Locate and identify every blood parasite.
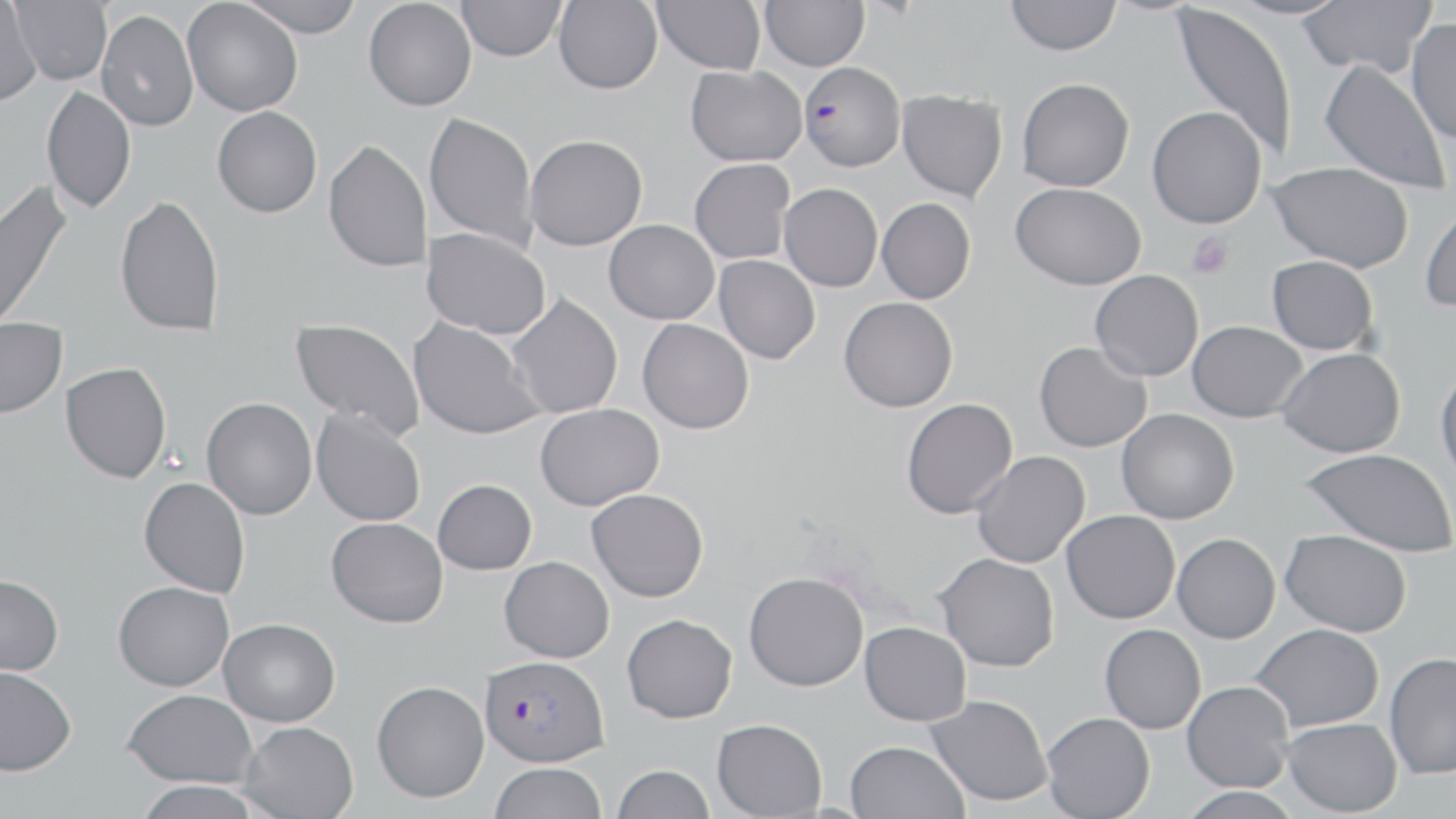
Approximate bounding boxes as (x1,y1)-(x2,y2) corner pairs in pixels.
Plasmodium falciparum-infected red blood cells: (798,61)-(905,171), (479,654)-(609,767).
No Plasmodium ovale, Plasmodium malariae, Plasmodium vivax, Babesia divergens, or Trypanosoma brucei observed.

Uninfected red blood cell locations: (182,0)-(303,116), (238,0)-(364,38), (363,0)-(476,111), (651,0)-(765,75), (760,0)-(869,71), (1005,0)-(1121,56), (1229,0)-(1349,20), (1297,0)-(1436,78), (9,1)-(112,85), (456,1)-(566,61), (553,1)-(662,94), (0,2)-(43,106), (1169,2)-(1297,162), (97,9)-(198,131), (1406,18)-(1456,144), (1319,60)-(1451,193), (685,65)-(806,166), (1016,77)-(1134,191), (41,84)-(136,214), (896,90)-(1008,202), (212,106)-(322,217), (1146,106)-(1267,228), (424,111)-(538,252), (525,134)-(647,251), (323,139)-(432,273), (689,158)-(795,264), (1269,161)-(1413,273), (0,178)-(72,333), (1010,182)-(1146,290), (779,183)-(883,292), (114,194)-(224,337), (876,198)-(976,303), (1419,198)-(1456,313), (604,219)-(719,324), (422,227)-(551,340), (714,255)-(820,364), (1267,255)-(1378,355), (1090,270)-(1203,381), (506,293)-(623,419), (839,296)-(958,412), (408,316)-(544,441), (289,317)-(426,440), (0,319)-(67,418), (637,319)-(754,434), (1187,320)-(1307,422), (1034,341)-(1152,452), (1277,347)-(1405,457), (60,362)-(171,483), (1435,366)-(1456,486), (201,397)-(317,519), (901,397)-(1017,519), (535,403)-(664,510), (311,408)-(426,527), (1116,409)-(1239,524), (1300,448)-(1456,557), (971,451)-(1090,568), (139,477)-(250,597), (433,479)-(537,574), (586,488)-(708,602), (1061,510)-(1180,624), (326,517)-(448,628), (1281,529)-(1411,636), (1172,533)-(1280,643), (935,553)-(1059,671), (499,556)-(614,662), (743,570)-(868,691), (0,574)-(64,676), (113,581)-(234,691), (622,613)-(737,723), (219,618)-(340,726), (859,621)-(971,726), (1099,623)-(1206,734), (1249,623)-(1384,732), (1384,651)-(1456,779), (0,666)-(76,775), (371,680)-(489,802), (1181,680)-(1293,792), (123,689)-(257,788), (926,694)-(1052,806), (1041,712)-(1155,819), (1282,717)-(1402,816), (712,718)-(827,818), (238,721)-(359,819), (845,740)-(968,819), (490,762)-(607,819), (611,764)-(715,819), (132,780)-(264,819), (1177,786)-(1302,819). Platelet locations: (1186,232)-(1233,279). Slide-level diagnosis: Plasmodium falciparum. May-Grünwald-Giemsa-stained preparation. Thin blood film. Optical microscopy. One field of a larger specimen. Image is 1456×819 pixels. 1000x magnification.